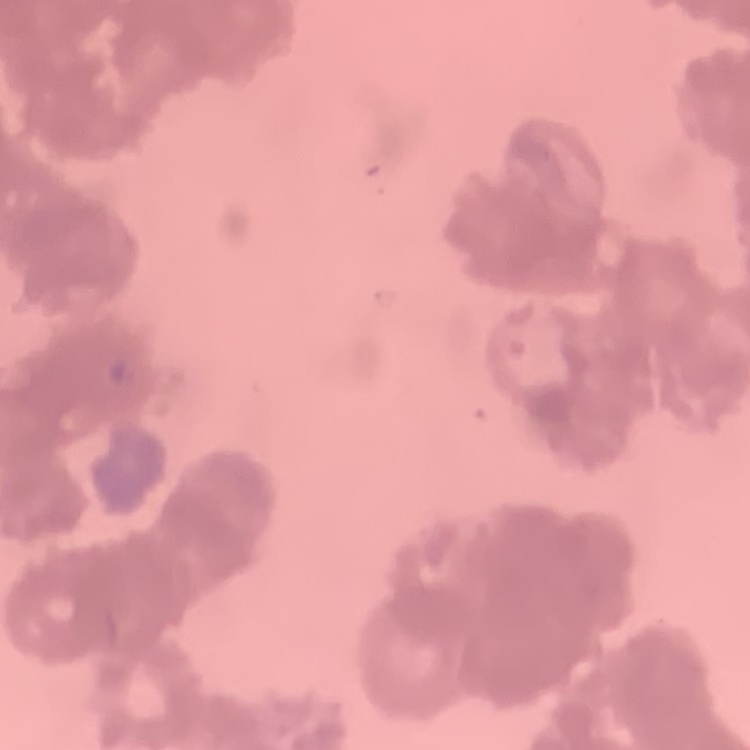
erythrocyte morphology = rouleaux formation
preparation = thin blood film
stain = Field's or Giemsa
image type = square crop of a larger photomicrograph